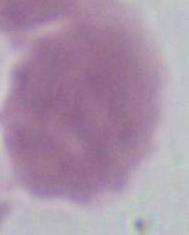
Summary:
  - Modality: photomicrograph
  - Identification: red blood cell
  - Magnification: 1000x